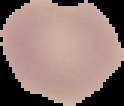

Summary:
  - Malaria status: uninfected
  - Preparation: thin blood film
  - Image size: 124×106 pixels
  - Image type: segmented cell region on a black background